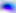 Toxoplasma gondii is shown. 400x magnification. Photomicrograph.